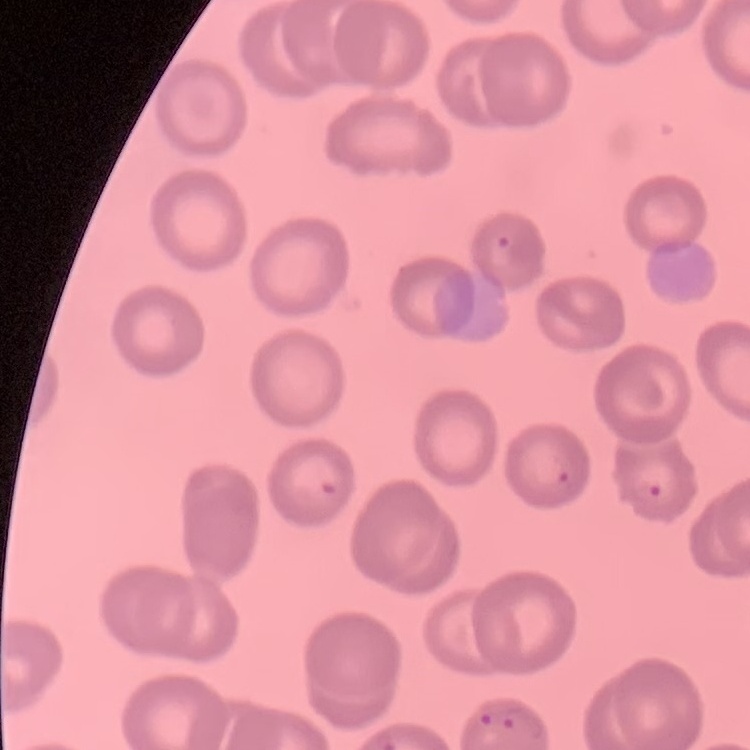
The erythrocytes show no rouleaux formation. Thin blood smear. Stained with either Field's or Giemsa. One tile cut from a larger photomicrograph.